Describe the morphology of the red blood cells.
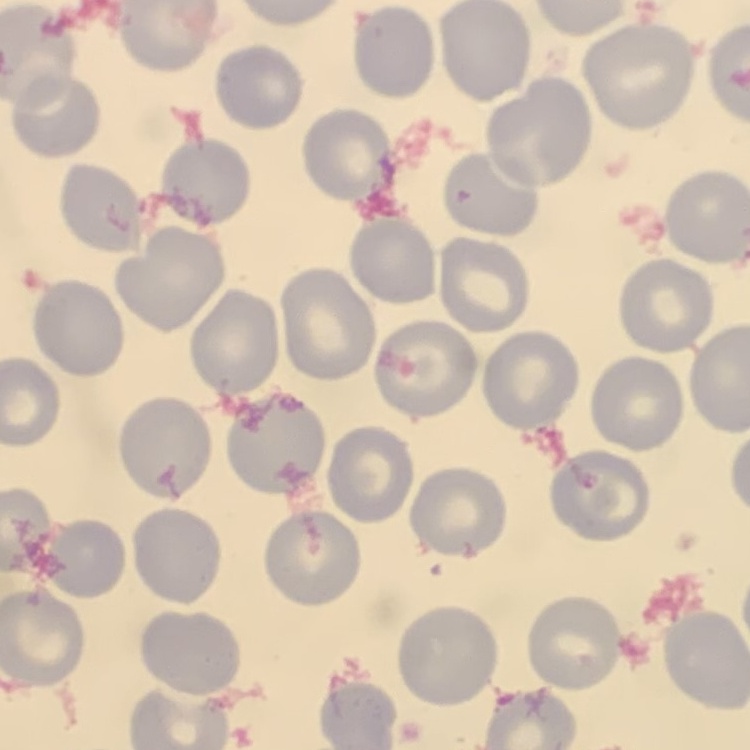

They show no rouleaux formation.

Summary:
  - Image type: square crop of a larger photomicrograph
  - Preparation: thin blood film
  - Stain: Field's or Giemsa